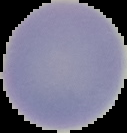
image size = 127×133 pixels
preparation = thin blood film
image type = segmented cell region with the area outside set to black
malaria status = uninfected